Locate every blood parasite and identify its species.
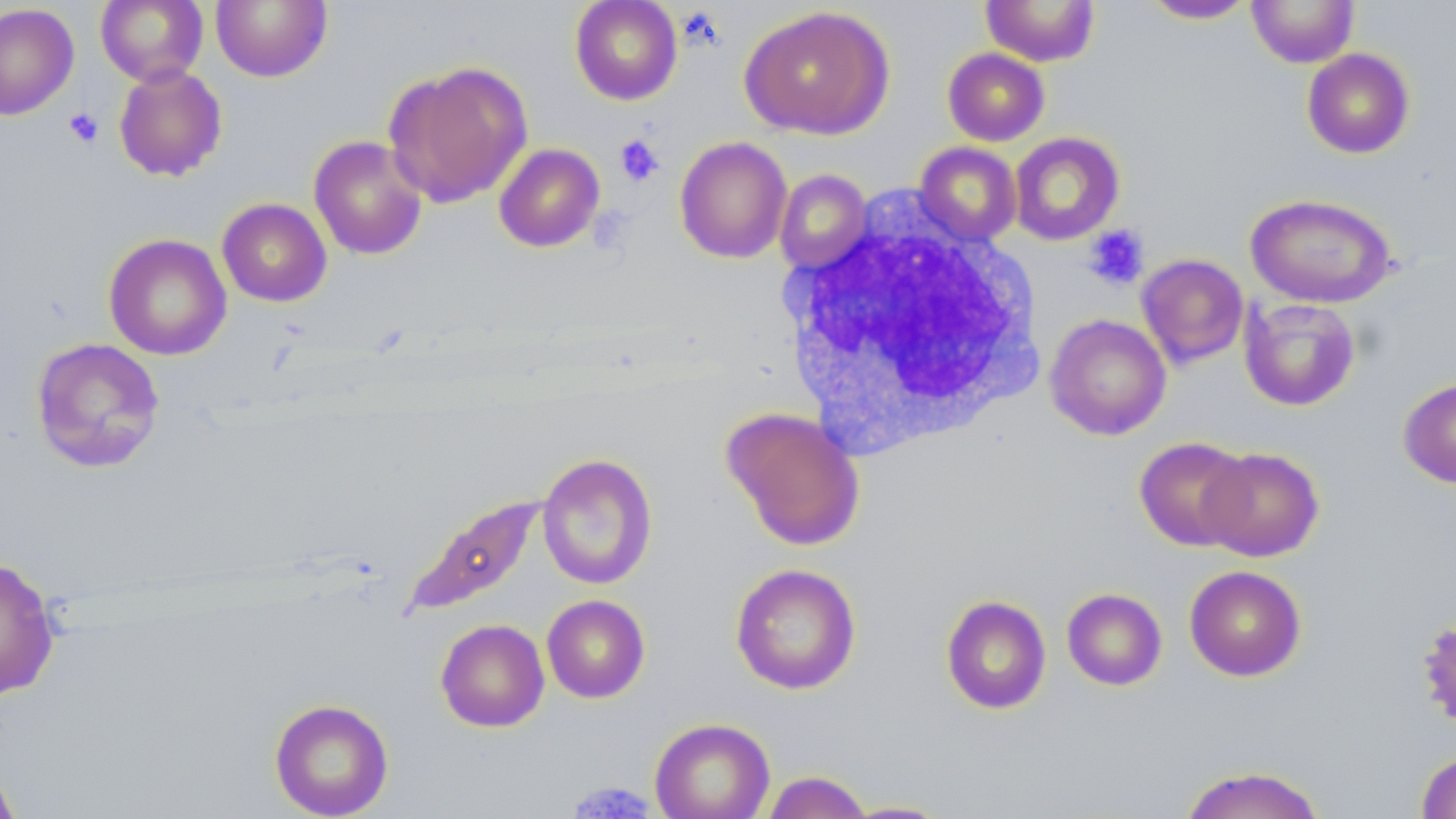

No blood parasites seen.

Summary:
  - Coordinate format: approximate bounding boxes as [x1, y1, x2, y2] in pixels
  - White blood cell locations: [782, 205, 1044, 458]
  - Platelet locations: [64, 107, 104, 149], [614, 134, 665, 187], [1082, 224, 1150, 291], [567, 780, 656, 818]
  - Uninfected red blood cell locations: [95, 0, 208, 86], [210, 0, 332, 83], [569, 0, 683, 105], [1246, 0, 1360, 67], [980, 1, 1101, 66], [1141, 1, 1258, 24], [0, 3, 79, 120], [739, 5, 894, 140], [942, 47, 1050, 146], [1301, 48, 1415, 159], [382, 60, 533, 208], [113, 63, 228, 182], [1009, 131, 1126, 245], [308, 135, 428, 260], [674, 136, 793, 264], [914, 142, 1022, 246], [493, 143, 605, 253], [775, 169, 873, 274], [1245, 193, 1398, 308], [217, 198, 332, 307], [103, 233, 232, 361], [1136, 253, 1250, 369], [1240, 298, 1361, 411], [1045, 313, 1172, 441], [30, 337, 165, 474], [1398, 376, 1456, 489], [721, 407, 866, 551], [1134, 436, 1252, 551], [1199, 446, 1324, 562], [537, 453, 658, 590], [404, 494, 548, 615], [0, 557, 60, 701], [730, 563, 861, 695], [1184, 565, 1307, 681], [1062, 588, 1167, 690], [542, 595, 650, 703], [940, 595, 1051, 715], [1416, 614, 1456, 731], [435, 618, 550, 733], [268, 698, 394, 819], [650, 717, 776, 819], [1415, 749, 1456, 818], [0, 758, 21, 819], [1178, 765, 1327, 819], [761, 771, 874, 818], [839, 800, 955, 818]
  - Slide-level diagnosis: negative for blood parasites
  - Stain: May-Grünwald-Giemsa
  - Image size: 1456×819 pixels
  - Magnification: 1000x
  - Field of view: one of a larger specimen
  - Preparation: thin blood film
  - Modality: light microscopy